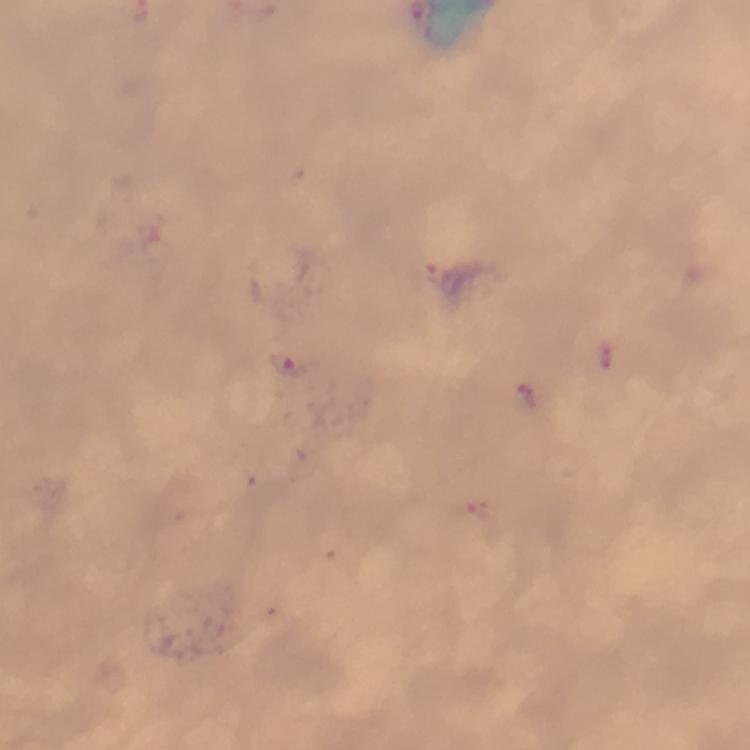
Approximate centers as [x, y] in pixels.
Summary:
  - Plasmodium parasite locations: [438, 275], [292, 364]
  - Cropped from: a single field of view
  - Magnification: 100x
  - Context: from a malaria diagnostic workup
  - Preparation: thick blood film
  - Capture: smartphone mounted on the microscope
  - Stain: Giemsa
  - Image size: 750×750 pixels
  - Immersion oil: applied